Assess the morphology of the erythrocytes.
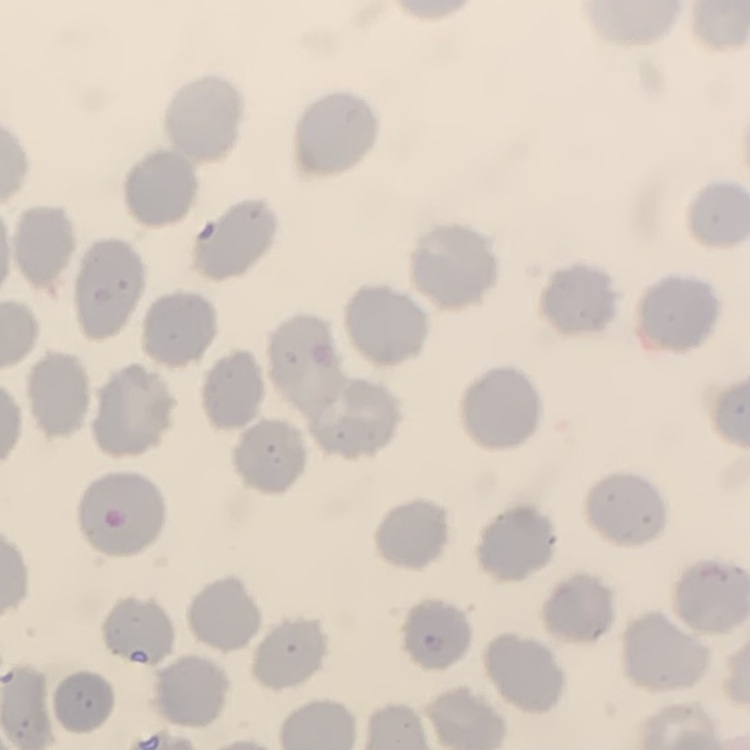
They show no rouleaux formation.

Summary:
  - Image type: square crop of a larger photomicrograph
  - Preparation: thin peripheral smear
  - Stain: Field's or Giemsa